Describe the morphology of the erythrocytes.
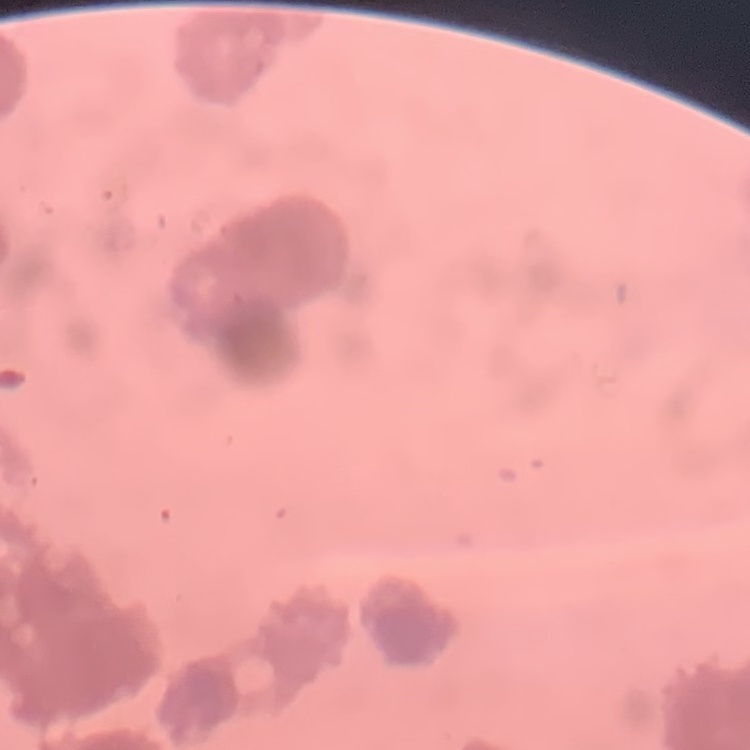
Rouleaux formation.

Square crop of a larger photomicrograph. Thin blood film. Stained with either Field's or Giemsa.